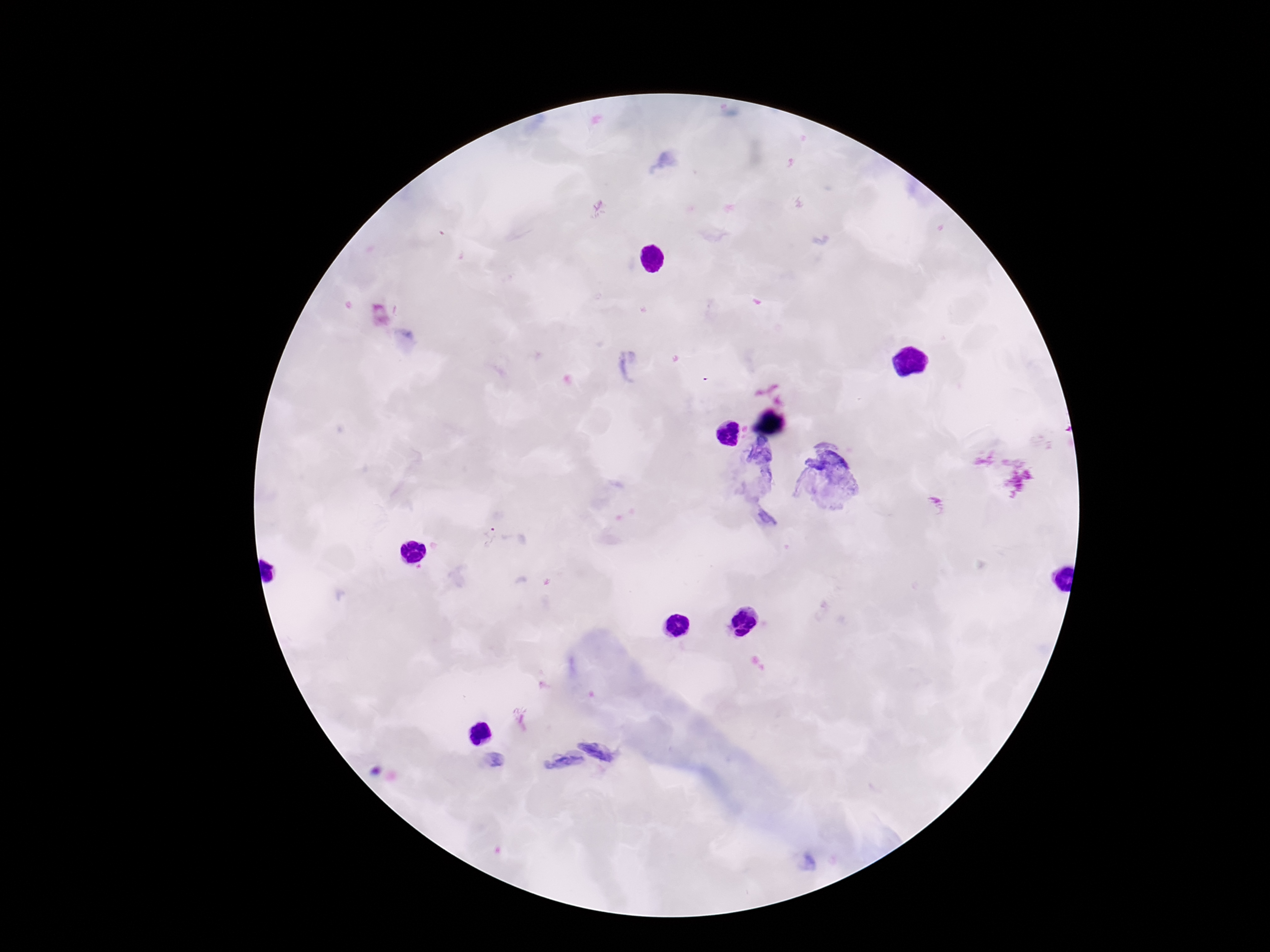
Approximate centers as (x, y) in pixels. Plasmodium parasite locations: (489, 537). Image is 1270×952 pixels. Giemsa-stained preparation. Thick blood smear. 100x magnification. Single field of view. Smartphone photograph taken through the microscope eyepiece. Patient malaria status: positive.